Give the position of every Plasmodium parasite visible.
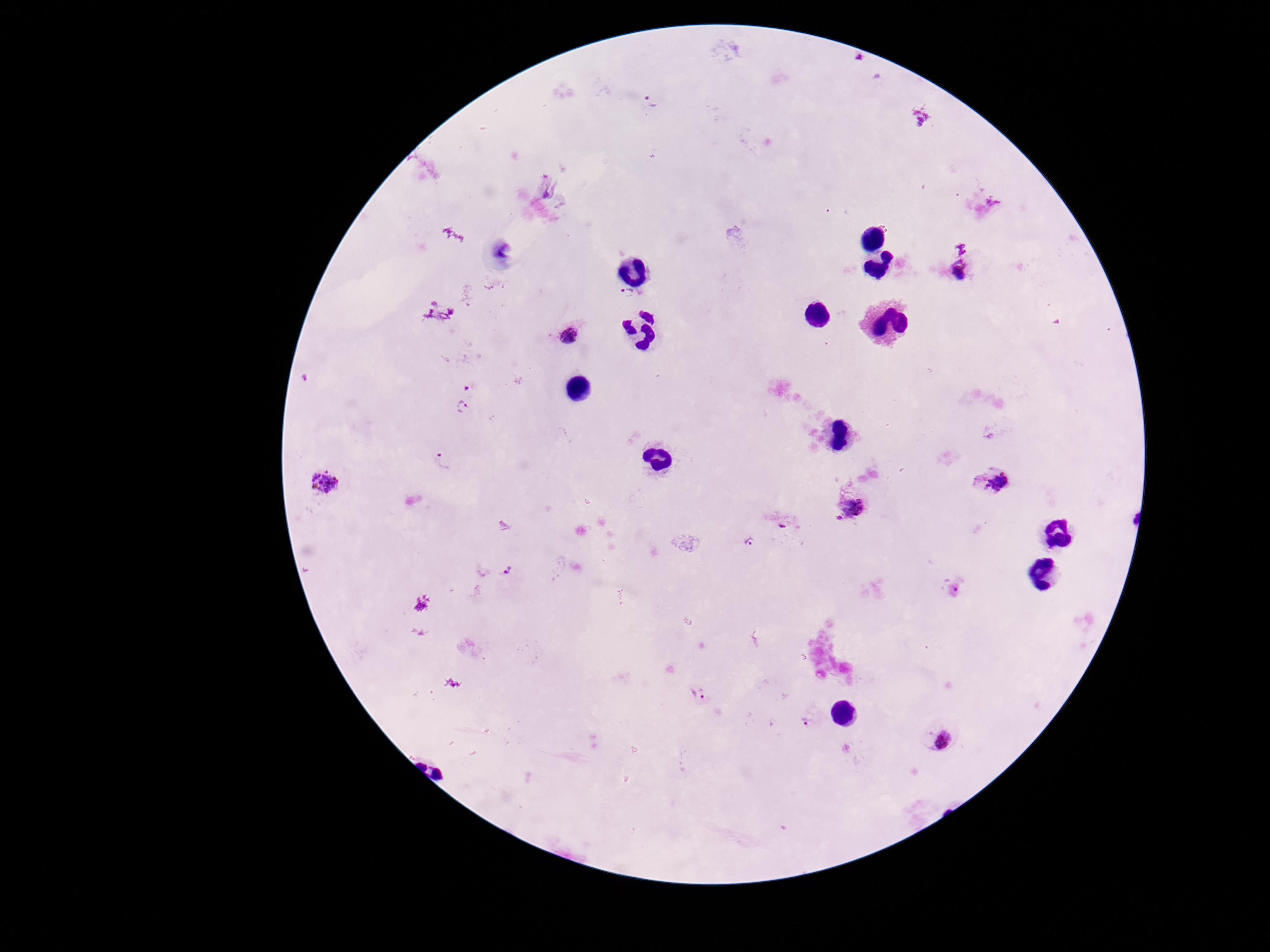
Approximate centers as (x, y) in pixels.
Plasmodium parasites: (652, 101), (960, 272), (627, 293), (569, 335), (305, 377), (462, 407), (442, 462), (326, 483), (998, 484), (853, 506), (784, 521), (750, 542), (506, 571), (700, 694), (807, 720), (944, 740).

Summary:
  - Capture: smartphone camera through the microscope eyepiece
  - Magnification: 100x
  - Field of view: one from this slide
  - Stain: Giemsa
  - Image size: 1270×952 pixels
  - Patient malaria status: positive
  - Preparation: thick blood film